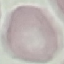
malaria status = uninfected
image type = cell patch, automatically extracted from a larger field of view and resized to 64 × 64 pixels
capture = smartphone through the microscope eyepiece
stain = Giemsa
preparation = thin blood film